Outline each P. falciparum parasite and classify it by life-cycle stage.
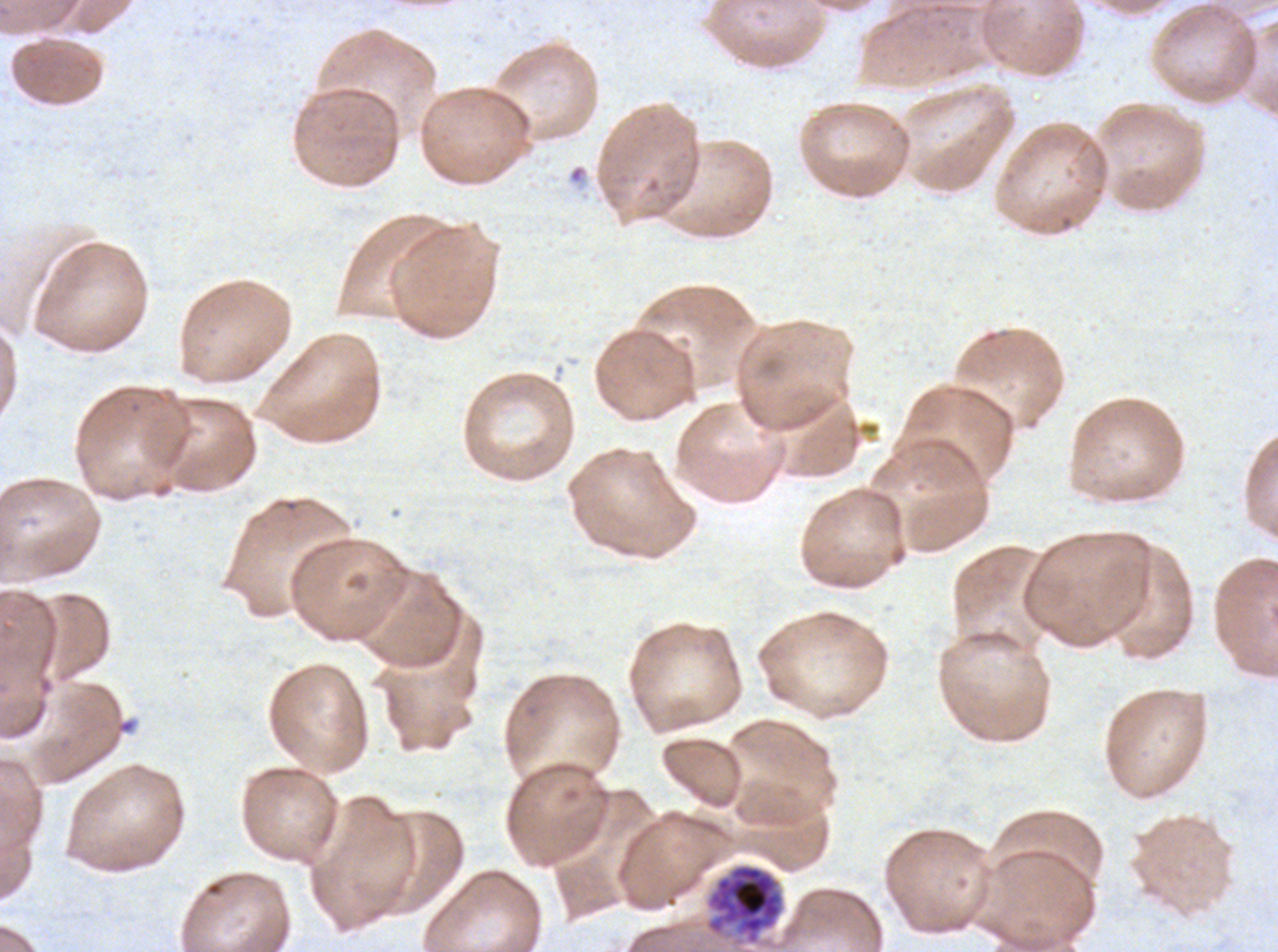
Approximate bounding boxes as {x1, y1, x2, y2} in pixels.
Late schizonts: {707, 864, 783, 944}.
No rings, late-ring/early-trophozoite forms, mid trophozoites, late trophozoites, early schizonts, segmenters, or gametocytes observed.

Giemsa stain. Thin blood film. Image is 1278×952 pixels. A sub-image separated from a larger composite. Ex-vivo P. falciparum culture from a patient in The Gambia, grown for 24 to 48 hours.